Identify the blood parasite species.
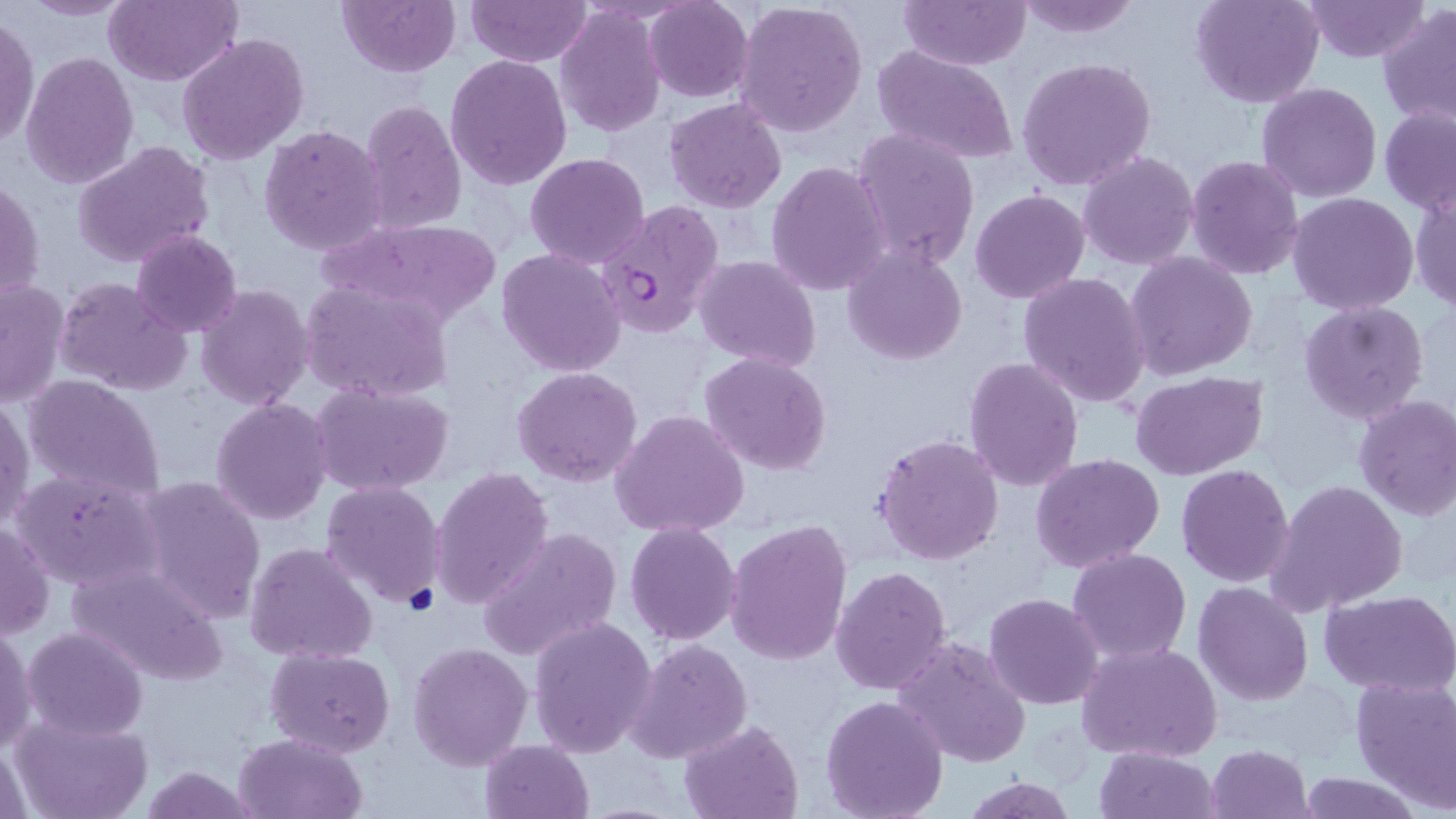
Plasmodium falciparum.

magnification = 1000x
preparation = thin blood smear
stain = May-Grünwald-Giemsa
image size = 1456×819 pixels
field of view = single
Plasmodium falciparum-infected red blood cell locations = approximate bounding boxes as [x1, y1, x2, y2] in pixels: [596, 202, 724, 340]
modality = light microscopy
uninfected red blood cell locations = approximate bounding boxes as [x1, y1, x2, y2] in pixels: [19, 0, 136, 21], [106, 0, 240, 86], [337, 0, 458, 76], [466, 0, 590, 66], [645, 0, 754, 102], [734, 0, 869, 139], [900, 0, 1031, 69], [1011, 0, 1143, 39], [1191, 0, 1324, 108], [1302, 0, 1431, 63], [1378, 4, 1456, 131], [555, 6, 665, 136], [0, 16, 39, 151], [177, 33, 309, 165], [872, 45, 1020, 167], [21, 51, 139, 191], [444, 54, 572, 192], [1016, 56, 1157, 192], [1256, 82, 1383, 202], [665, 97, 788, 212], [359, 98, 468, 235], [1379, 106, 1456, 218], [258, 123, 388, 255], [851, 127, 980, 272], [72, 141, 214, 269], [1078, 151, 1199, 271], [524, 152, 650, 270], [1185, 155, 1305, 280], [766, 161, 892, 298], [1, 175, 45, 307], [1409, 185, 1456, 313], [969, 189, 1090, 304], [1288, 193, 1419, 314], [318, 216, 505, 331], [131, 229, 241, 336], [843, 247, 968, 365], [496, 248, 625, 376], [1126, 252, 1258, 380], [694, 255, 821, 370], [1017, 272, 1150, 409], [53, 276, 191, 397], [0, 279, 67, 409], [301, 279, 452, 404], [196, 283, 313, 410], [1299, 300, 1429, 424], [700, 351, 834, 476], [964, 356, 1085, 492], [512, 366, 643, 486], [1130, 370, 1266, 479], [23, 374, 167, 502], [313, 384, 452, 495], [0, 393, 34, 533], [1353, 394, 1456, 522], [210, 397, 335, 524], [610, 408, 753, 538], [873, 432, 1005, 565], [1031, 453, 1165, 573], [1176, 463, 1295, 586], [429, 465, 553, 610], [10, 468, 163, 596], [136, 475, 268, 624], [321, 479, 448, 610], [1267, 479, 1410, 616], [0, 520, 53, 640], [726, 520, 853, 667], [625, 523, 741, 645], [477, 529, 620, 661], [244, 541, 378, 666], [1067, 547, 1192, 664], [65, 560, 230, 688], [831, 567, 953, 693], [1193, 582, 1314, 705], [1322, 589, 1456, 695], [983, 592, 1105, 710], [529, 616, 658, 759], [0, 625, 37, 757], [21, 626, 148, 742], [627, 636, 751, 766], [893, 637, 1032, 768], [1077, 640, 1223, 763], [407, 641, 533, 772], [267, 647, 395, 757], [1351, 675, 1456, 811], [819, 694, 948, 819], [9, 715, 154, 819], [677, 718, 804, 819], [232, 732, 368, 819], [1, 740, 32, 819], [480, 740, 594, 818], [1207, 743, 1313, 819], [1094, 747, 1218, 819], [133, 764, 267, 819], [1298, 773, 1424, 817], [955, 775, 1082, 819]